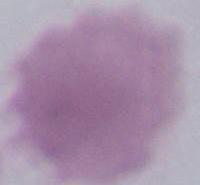

Micrograph. An erythrocyte is shown. 1000x magnification.